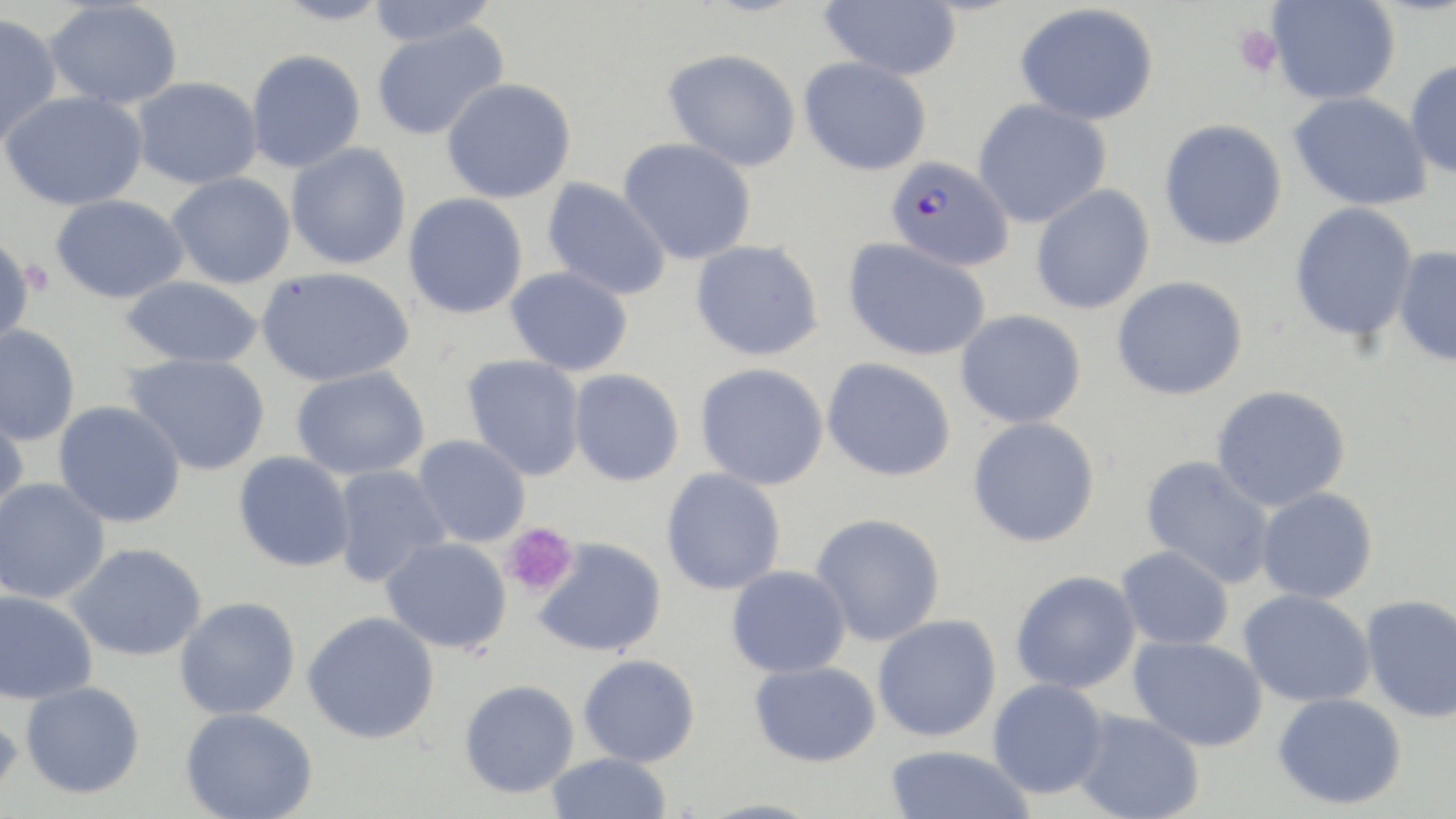
slide-level diagnosis = Plasmodium falciparum
uninfected red blood cell locations = approximate bounding boxes as (x1,y1)-(x2,y2) corner pairs in pixels: (273,0)-(391,26), (365,0)-(500,47), (819,0)-(962,80), (1266,0)-(1400,105), (44,1)-(183,109), (1015,3)-(1159,126), (0,12)-(62,148), (371,20)-(509,142), (664,48)-(802,172), (246,49)-(366,173), (799,57)-(932,176), (1405,59)-(1456,178), (131,76)-(262,189), (442,78)-(576,203), (1,90)-(149,210), (1289,91)-(1432,211), (973,97)-(1112,228), (1159,119)-(1288,250), (618,137)-(757,265), (286,142)-(412,270), (166,172)-(296,289), (542,178)-(671,301), (1031,184)-(1155,315), (403,193)-(528,319), (51,194)-(190,304), (1289,201)-(1419,342), (0,232)-(34,352), (843,237)-(991,362), (691,239)-(824,361), (1393,246)-(1456,367), (505,266)-(633,376), (257,267)-(415,387), (120,276)-(265,369), (1112,276)-(1248,401), (955,309)-(1086,428), (0,324)-(81,446), (123,353)-(272,476), (462,354)-(586,481), (822,357)-(956,482), (695,363)-(829,490), (291,365)-(430,480), (568,368)-(685,486), (1210,385)-(1351,513), (54,400)-(186,528), (0,404)-(29,521), (968,416)-(1100,548), (413,435)-(531,548), (234,451)-(355,572), (1140,455)-(1277,589), (331,464)-(450,587), (661,468)-(786,595), (0,478)-(111,604), (1256,487)-(1378,604), (811,513)-(946,646), (381,536)-(512,653), (532,537)-(667,657), (65,542)-(207,662), (1116,545)-(1234,650), (727,565)-(851,678), (1010,570)-(1141,694), (0,589)-(98,705), (1238,589)-(1375,708), (1361,594)-(1456,723), (175,596)-(301,720), (302,611)-(440,743), (872,614)-(1002,742), (1129,636)-(1267,751), (579,653)-(700,767), (749,660)-(881,767), (987,678)-(1108,799), (459,679)-(579,797), (20,681)-(145,798), (1272,692)-(1408,809), (0,702)-(24,812), (180,706)-(318,819), (1073,708)-(1204,819), (884,745)-(1035,819), (546,752)-(672,818)
image size = 1456×819 pixels
field of view = one of a larger specimen
preparation = thin blood film
magnification = 1000x
stain = May-Grünwald-Giemsa
platelet locations = approximate bounding boxes as (x1,y1)-(x2,y2) corner pairs in pixels: (1232,24)-(1283,79), (18,259)-(56,299), (502,522)-(578,599)
modality = light microscopy
Plasmodium falciparum-infected red blood cell locations = approximate bounding boxes as (x1,y1)-(x2,y2) corner pairs in pixels: (885,156)-(1014,272)